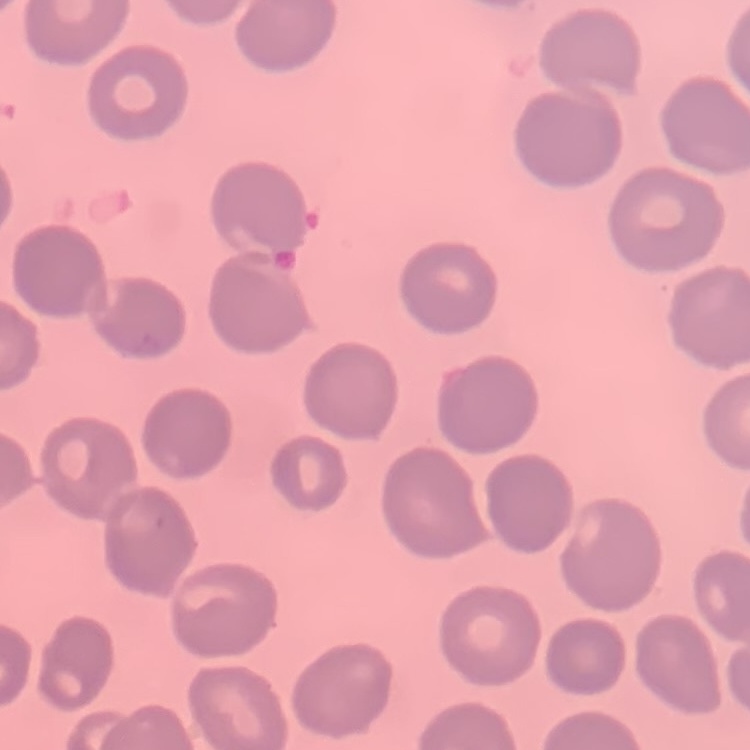

erythrocyte morphology = no rouleaux formation
image type = square crop of a larger photomicrograph
preparation = thin peripheral smear
stain = Field's or Giemsa